Identify the parasite.
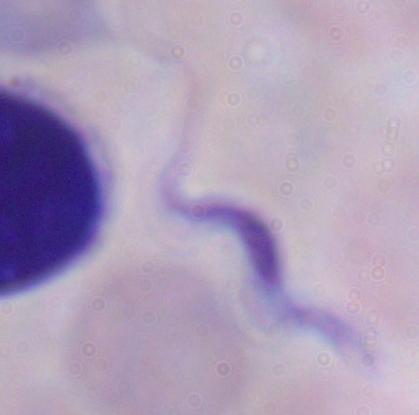

A trypanosome.

1000x magnification. Photomicrograph.